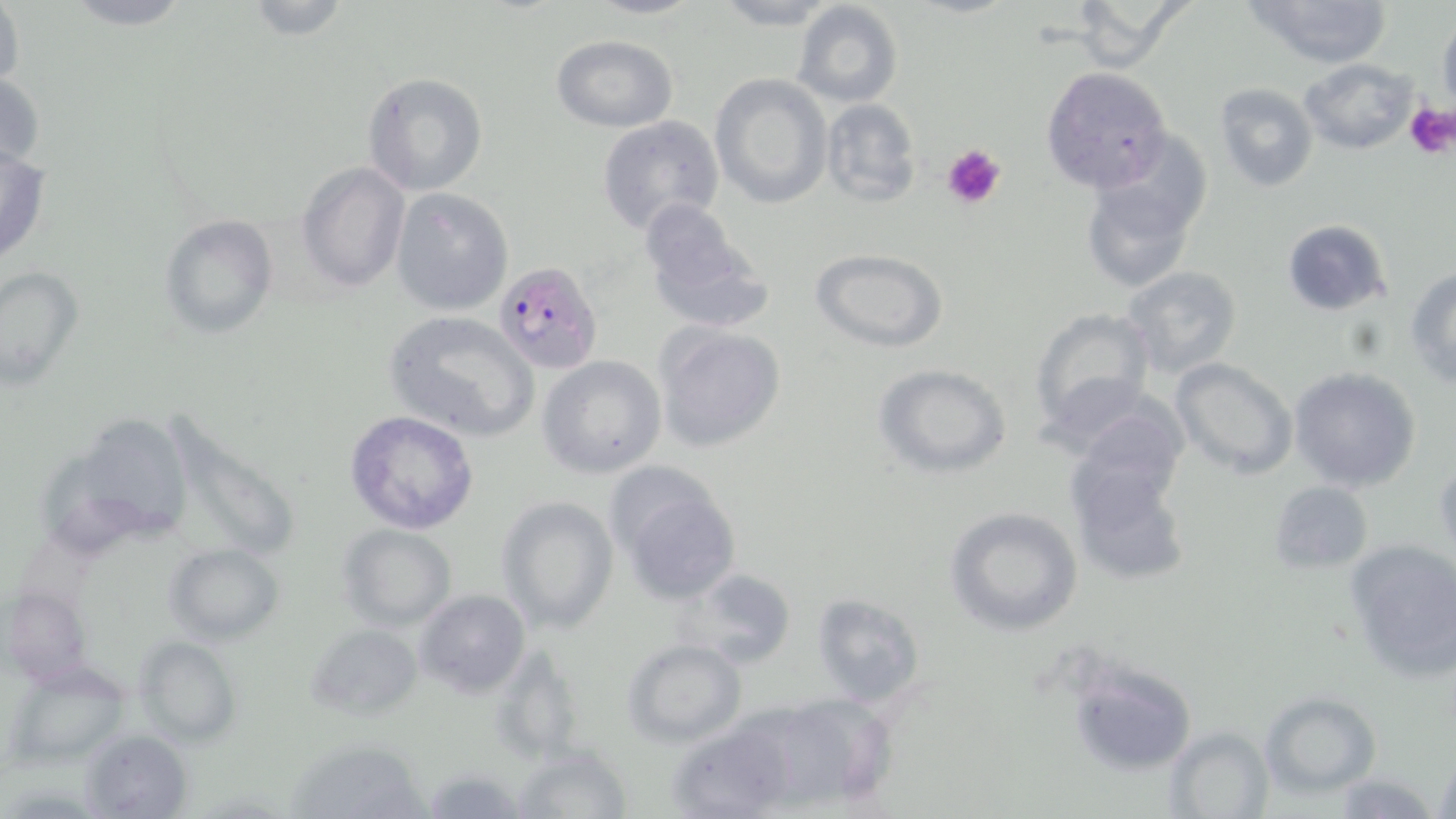 Approximate bounding boxes as named x1/y1/x2/y2 corners in pixels. Plasmodium falciparum-infected red blood cell locations: (x1=495, y1=260, x2=602, y2=374). Platelet locations: (x1=1406, y1=100, x2=1456, y2=157), (x1=941, y1=143, x2=1007, y2=209). Uninfected red blood cell locations: (x1=0, y1=0, x2=24, y2=95), (x1=57, y1=0, x2=198, y2=31), (x1=239, y1=0, x2=353, y2=40), (x1=585, y1=0, x2=705, y2=20), (x1=710, y1=0, x2=842, y2=30), (x1=1063, y1=0, x2=1192, y2=73), (x1=1243, y1=0, x2=1393, y2=71), (x1=791, y1=2, x2=903, y2=109), (x1=1437, y1=16, x2=1456, y2=111), (x1=551, y1=36, x2=678, y2=131), (x1=1299, y1=58, x2=1419, y2=155), (x1=1043, y1=67, x2=1171, y2=193), (x1=0, y1=71, x2=46, y2=173), (x1=361, y1=71, x2=487, y2=196), (x1=710, y1=75, x2=833, y2=208), (x1=1213, y1=83, x2=1319, y2=194), (x1=819, y1=98, x2=922, y2=208), (x1=596, y1=114, x2=724, y2=236), (x1=0, y1=146, x2=51, y2=267), (x1=297, y1=161, x2=412, y2=295), (x1=1082, y1=167, x2=1205, y2=293), (x1=391, y1=187, x2=513, y2=316), (x1=637, y1=199, x2=774, y2=334), (x1=161, y1=214, x2=278, y2=339), (x1=1281, y1=219, x2=1393, y2=316), (x1=811, y1=249, x2=950, y2=351), (x1=1, y1=265, x2=83, y2=387), (x1=1122, y1=266, x2=1245, y2=380), (x1=1406, y1=266, x2=1456, y2=388), (x1=1028, y1=305, x2=1157, y2=439), (x1=383, y1=309, x2=542, y2=442), (x1=653, y1=322, x2=787, y2=453), (x1=538, y1=354, x2=668, y2=479), (x1=1169, y1=358, x2=1297, y2=479), (x1=875, y1=364, x2=1013, y2=480), (x1=1288, y1=367, x2=1422, y2=493), (x1=1066, y1=400, x2=1190, y2=516), (x1=176, y1=409, x2=303, y2=552), (x1=97, y1=410, x2=191, y2=541), (x1=344, y1=411, x2=480, y2=535), (x1=46, y1=444, x2=130, y2=554), (x1=1433, y1=457, x2=1456, y2=561), (x1=1068, y1=463, x2=1190, y2=586), (x1=607, y1=464, x2=744, y2=608), (x1=1270, y1=480, x2=1373, y2=574), (x1=497, y1=495, x2=619, y2=633), (x1=944, y1=505, x2=1083, y2=636), (x1=337, y1=524, x2=457, y2=632), (x1=1344, y1=538, x2=1456, y2=679), (x1=166, y1=544, x2=285, y2=642), (x1=681, y1=568, x2=798, y2=668), (x1=2, y1=585, x2=89, y2=687), (x1=414, y1=588, x2=530, y2=698), (x1=810, y1=594, x2=924, y2=708), (x1=306, y1=623, x2=422, y2=722), (x1=137, y1=636, x2=241, y2=746), (x1=621, y1=638, x2=747, y2=748), (x1=491, y1=641, x2=587, y2=767), (x1=1068, y1=659, x2=1202, y2=780), (x1=5, y1=663, x2=129, y2=768), (x1=1262, y1=691, x2=1380, y2=798), (x1=668, y1=716, x2=797, y2=819), (x1=1165, y1=726, x2=1273, y2=817), (x1=81, y1=728, x2=192, y2=818), (x1=284, y1=738, x2=429, y2=818), (x1=513, y1=744, x2=629, y2=818), (x1=1433, y1=751, x2=1456, y2=819), (x1=426, y1=767, x2=522, y2=819), (x1=1327, y1=774, x2=1439, y2=817). Slide-level diagnosis: Plasmodium falciparum. May-Grünwald-Giemsa-stained preparation. Captured at 1000x magnification. Optical microscopy. Image is 1456×819 pixels. Thin blood film. Single field of view.